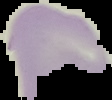

From a thin blood film. Result: negative for malaria parasites. Cell region segmented out of the field of view; the surrounding area is masked to black. Image is 112×100 pixels.